Identify the parasite.
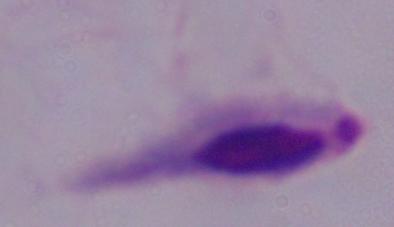
This is a trichomonad.

magnification = 1000x
modality = photomicrograph